Name the parasite shown.
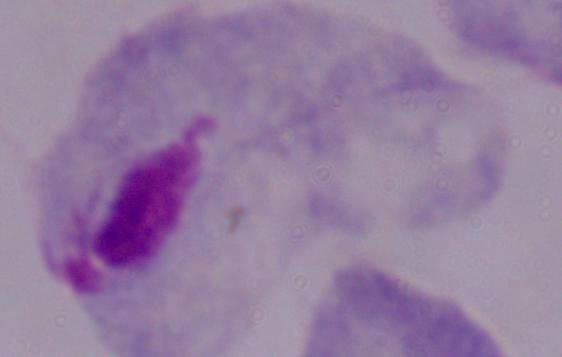

This is a trichomonad.

Summary:
  - Modality: photomicrograph
  - Magnification: 1000x